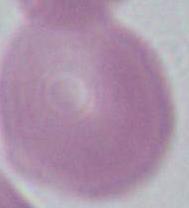
Summary:
  - Modality: micrograph
  - Identification: red blood cell
  - Magnification: 1000x